Identify the preparation type.
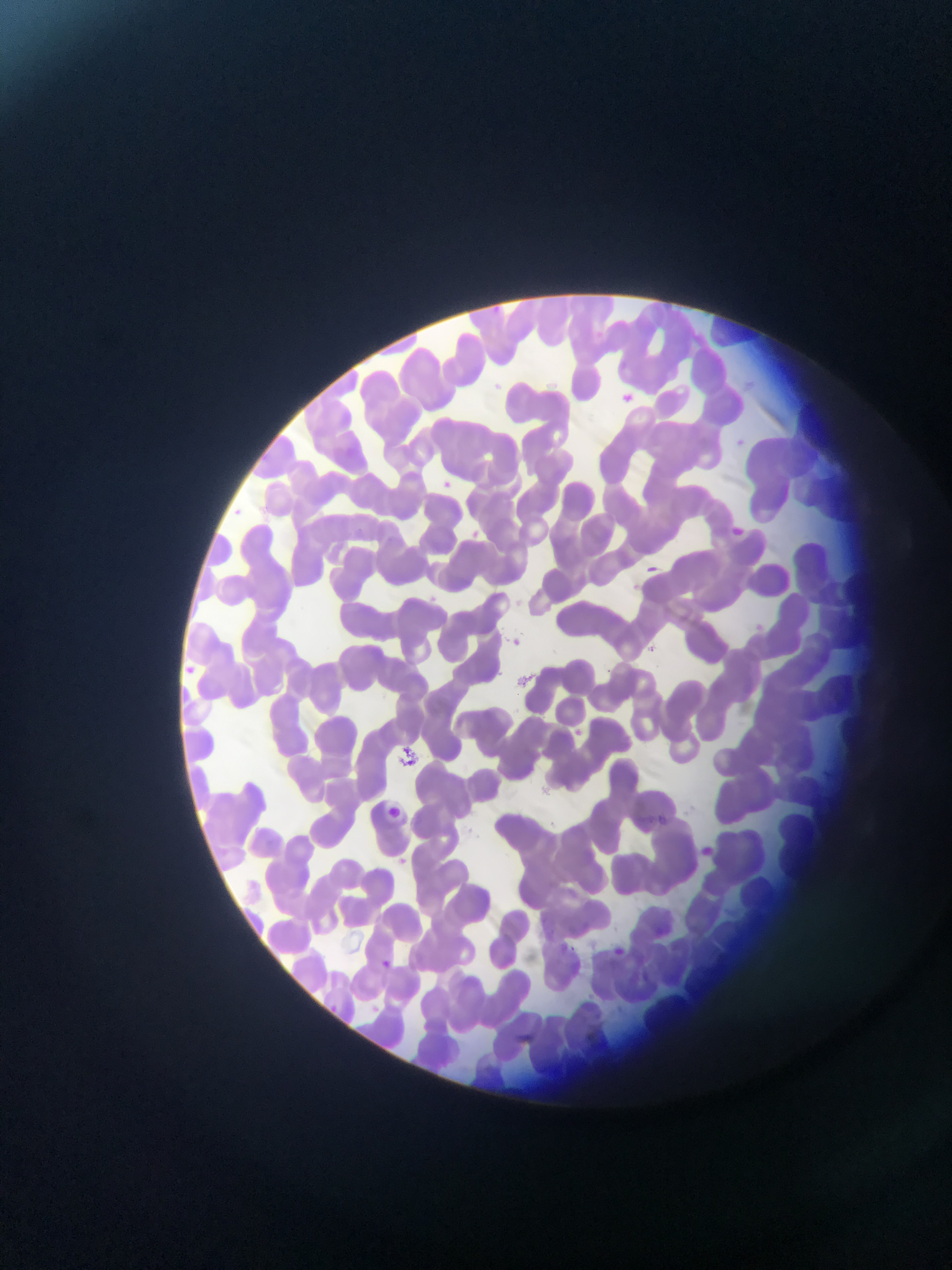

Thin blood smear.

Approximate bounding boxes as (left, top, right, bottom) in pixels.
Summary:
  - Plasmodium parasite locations: (491, 302, 503, 315), (586, 321, 610, 351), (495, 380, 507, 397), (624, 386, 639, 410), (735, 437, 743, 449), (261, 455, 275, 466), (443, 479, 458, 496), (228, 507, 245, 519), (735, 522, 755, 542), (356, 524, 364, 534), (338, 529, 347, 540), (471, 530, 491, 545), (444, 538, 460, 553), (641, 561, 669, 575), (428, 592, 440, 605), (751, 621, 763, 634), (510, 629, 529, 649), (648, 641, 662, 653), (181, 657, 215, 690), (573, 726, 590, 743), (397, 731, 425, 778), (255, 798, 277, 817), (390, 802, 410, 834), (640, 809, 670, 830), (657, 810, 673, 822), (697, 843, 727, 861), (653, 917, 674, 947), (564, 942, 582, 959), (608, 943, 623, 953), (372, 953, 396, 973), (640, 966, 653, 982), (320, 994, 340, 1014), (370, 1002, 391, 1020), (514, 1030, 544, 1047)
  - Image size: 952×1270 pixels
  - Field of view: single
  - Country: Ghana
  - Capture: mobile-phone photograph through a microscope